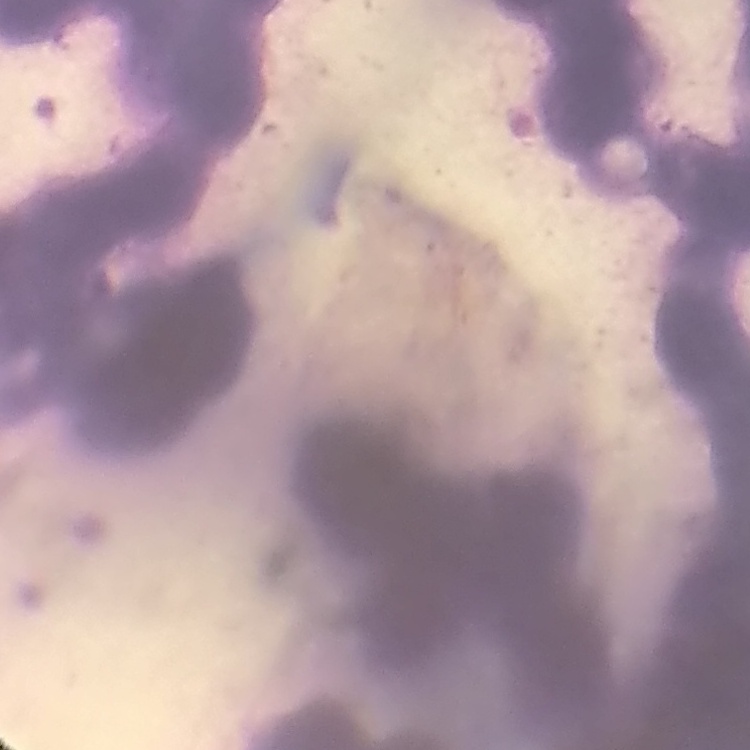
red_blood_cell_morphology: rouleaux formation
image_type: square crop of a larger photomicrograph
stain: Field's or Giemsa
preparation: thin blood film